Comment on the morphology of the erythrocytes.
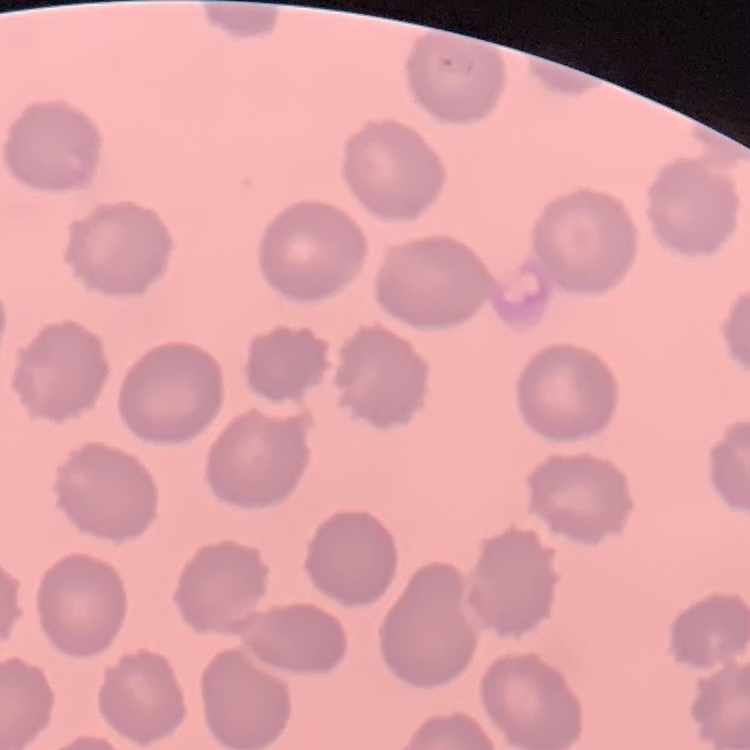

No rouleaux formation.

Summary:
  - Stain: Field's or Giemsa
  - Image type: square crop of a larger photomicrograph
  - Preparation: thin peripheral smear